Locate and identify every blood parasite.
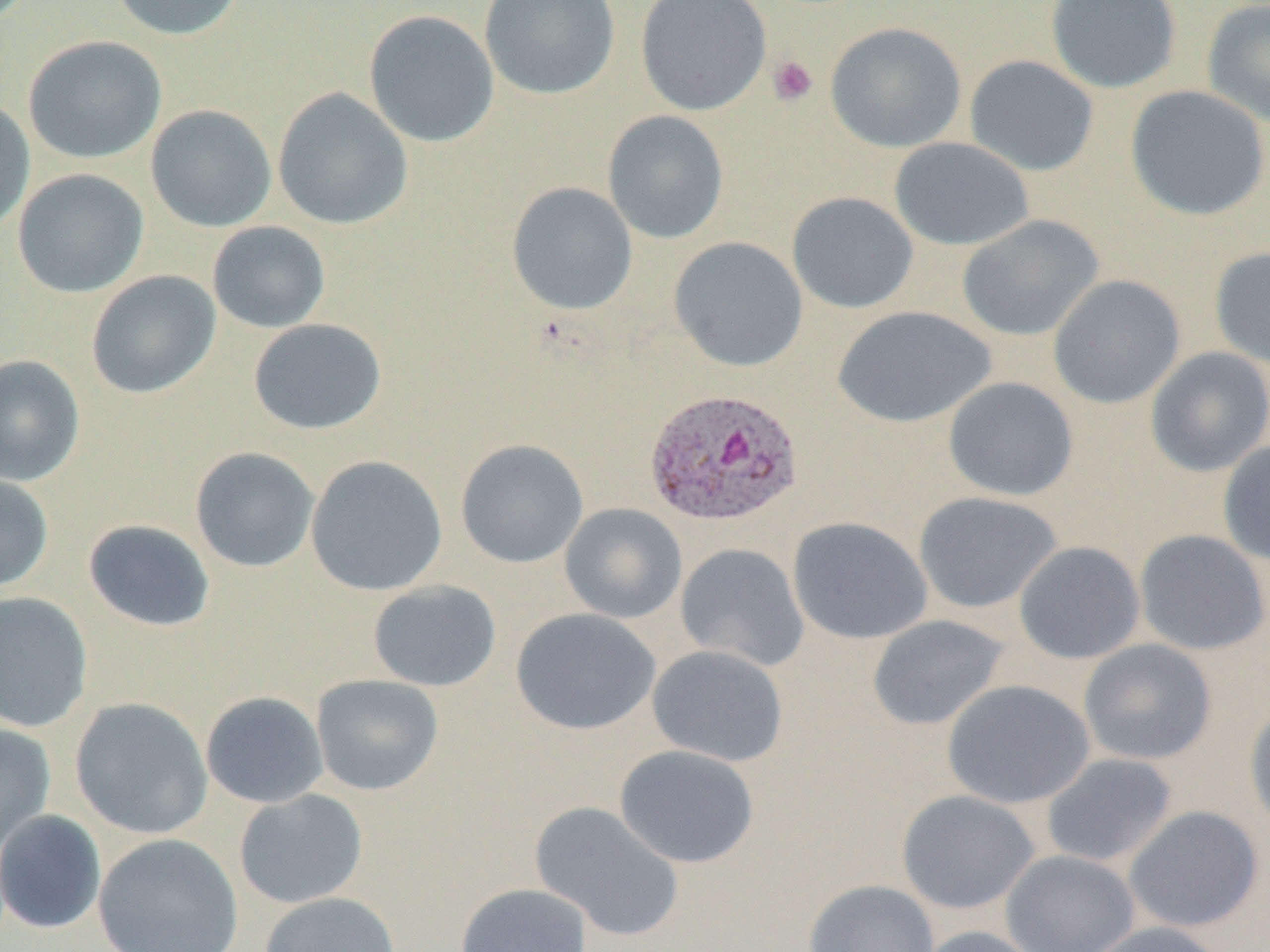

Approximate bounding boxes as (x1,y1)-(x2,y2) corner pairs in pixels.
Plasmodium ovale-infected red blood cells: (644,386)-(805,527).
No Plasmodium falciparum, Plasmodium malariae, Plasmodium vivax, Babesia divergens, or Trypanosoma brucei observed.

Platelet locations: (767,54)-(818,107). Uninfected red blood cell locations: (107,0)-(246,41), (479,0)-(620,99), (635,0)-(772,116), (1045,0)-(1182,93), (1201,0)-(1270,128), (364,10)-(499,147), (825,22)-(967,153), (23,35)-(167,164), (964,55)-(1100,176), (1125,85)-(1269,221), (272,88)-(413,230), (0,98)-(35,236), (145,105)-(277,232), (602,110)-(729,244), (889,137)-(1034,251), (12,168)-(149,298), (506,182)-(638,315), (787,192)-(919,314), (957,214)-(1104,341), (207,221)-(330,333), (668,236)-(808,372), (1209,246)-(1270,369), (86,270)-(221,399), (1048,275)-(1185,408), (832,306)-(996,428), (248,318)-(387,435), (1144,346)-(1270,478), (0,354)-(86,486), (942,377)-(1079,501), (455,438)-(589,569), (1217,440)-(1270,566), (190,447)-(320,573), (305,455)-(448,596), (0,474)-(54,593), (913,491)-(1063,614), (559,503)-(687,624), (787,516)-(932,645), (83,519)-(216,632), (1134,529)-(1270,656), (1013,541)-(1145,664), (675,543)-(809,672), (367,580)-(501,692), (0,591)-(93,733), (510,608)-(661,735), (867,614)-(1011,730), (1078,639)-(1217,765), (647,645)-(789,767), (311,674)-(444,795), (941,679)-(1095,810), (200,691)-(329,808), (69,697)-(213,840), (1244,701)-(1270,838), (0,721)-(55,855), (614,744)-(760,868), (1040,753)-(1178,868), (234,789)-(368,909), (896,790)-(1041,915), (529,801)-(685,942), (1123,805)-(1264,933), (0,809)-(107,935), (93,833)-(243,952), (1000,849)-(1140,952), (802,879)-(939,952), (455,883)-(593,952), (258,891)-(401,952), (1079,921)-(1231,952), (913,925)-(1044,952). Slide-level diagnosis: Plasmodium ovale. Single field of view. Image is 1270×952 pixels. Thin blood film. Light microscopy. 1000x magnification.